Locate every blood parasite and identify its species.
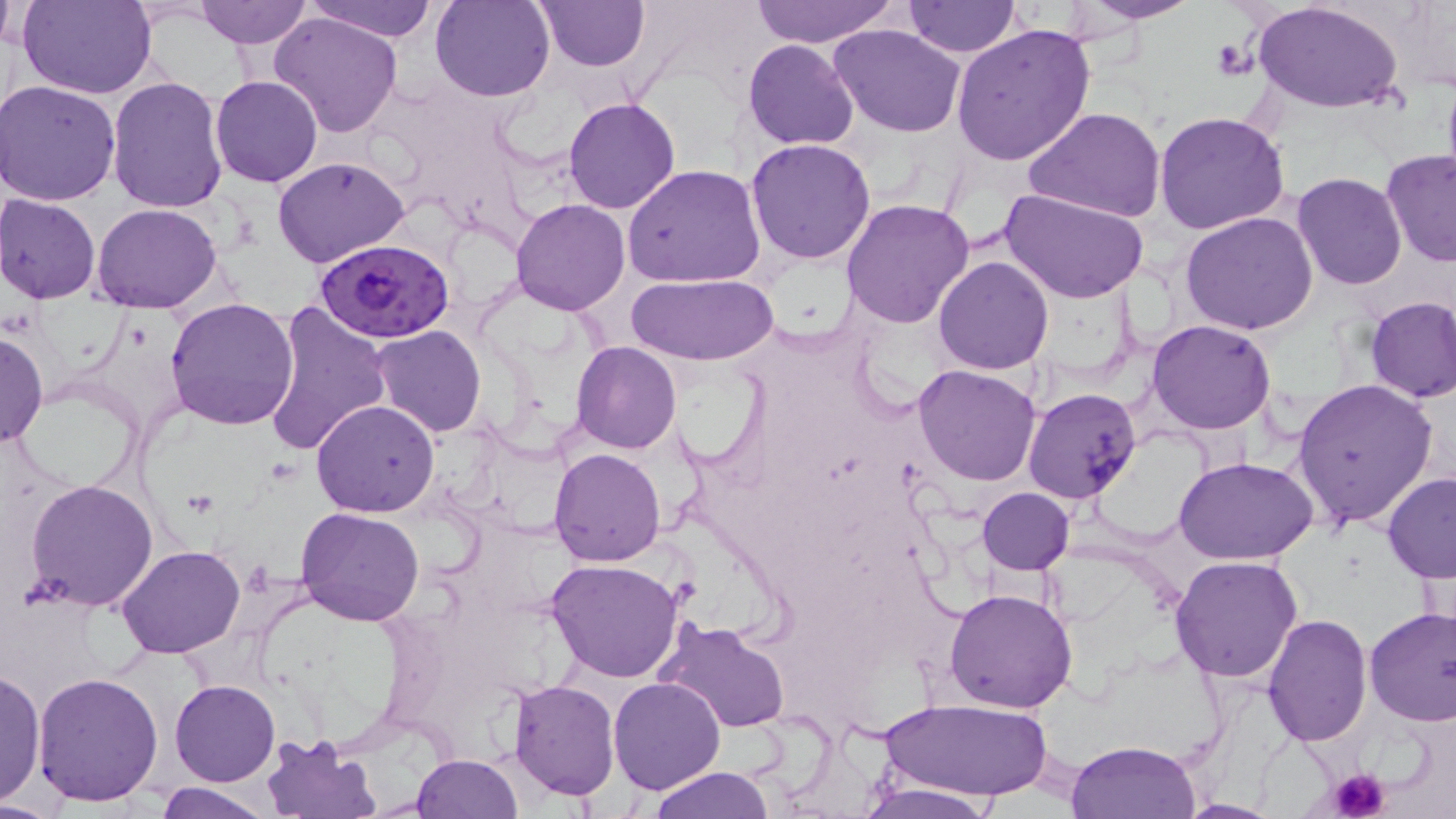

Approximate bounding boxes as (x1,y1)-(x2,y2) corner pairs in pixels.
Plasmodium falciparum-infected red blood cells: (317,239)-(454,344).
No Plasmodium ovale, Plasmodium malariae, Plasmodium vivax, Babesia divergens, or Trypanosoma brucei observed.

Summary:
  - Platelet locations: (1210,41)-(1256,78), (1328,765)-(1392,819)
  - Uninfected red blood cell locations: (20,0)-(156,98), (193,0)-(311,49), (304,0)-(440,42), (432,0)-(555,101), (536,0)-(648,71), (903,0)-(1019,58), (1076,0)-(1203,24), (750,1)-(898,46), (1252,2)-(1401,113), (0,5)-(21,53), (270,11)-(403,139), (951,23)-(1097,165), (829,24)-(966,137), (743,40)-(858,150), (209,74)-(323,188), (107,75)-(231,214), (0,80)-(122,205), (563,97)-(680,214), (1026,108)-(1168,222), (1154,110)-(1291,235), (746,138)-(877,264), (1380,149)-(1456,268), (272,156)-(409,269), (622,164)-(765,288), (1293,172)-(1407,290), (1000,187)-(1151,305), (0,194)-(102,304), (510,198)-(630,315), (840,198)-(974,328), (91,202)-(222,313), (1181,211)-(1318,335), (933,255)-(1054,374), (625,272)-(778,364), (1364,296)-(1456,403), (165,297)-(299,431), (260,300)-(392,458), (1148,320)-(1276,435), (371,325)-(487,437), (0,330)-(48,448), (571,342)-(681,453), (912,364)-(1042,485), (1291,376)-(1440,530), (1022,387)-(1142,504), (311,400)-(440,517), (549,447)-(666,565), (1178,458)-(1316,567), (1381,473)-(1456,581), (26,478)-(160,612), (977,487)-(1074,574), (294,508)-(424,626), (117,546)-(244,659), (1169,555)-(1303,684), (546,560)-(685,683), (944,588)-(1079,713), (1363,607)-(1456,727), (1263,613)-(1371,744), (657,620)-(791,733), (1,666)-(45,807), (33,673)-(164,807), (608,675)-(725,794), (508,678)-(620,801), (170,679)-(280,786), (879,697)-(1051,802), (260,733)-(379,818), (1065,738)-(1202,818), (413,753)-(523,818), (647,767)-(775,819), (154,781)-(273,818), (849,783)-(1005,818), (1175,800)-(1286,819)
  - Slide-level diagnosis: Plasmodium falciparum
  - Magnification: 1000x
  - Field of view: single
  - Modality: light microscopy
  - Preparation: thin blood smear
  - Image size: 1456×819 pixels
  - Stain: May-Grünwald-Giemsa